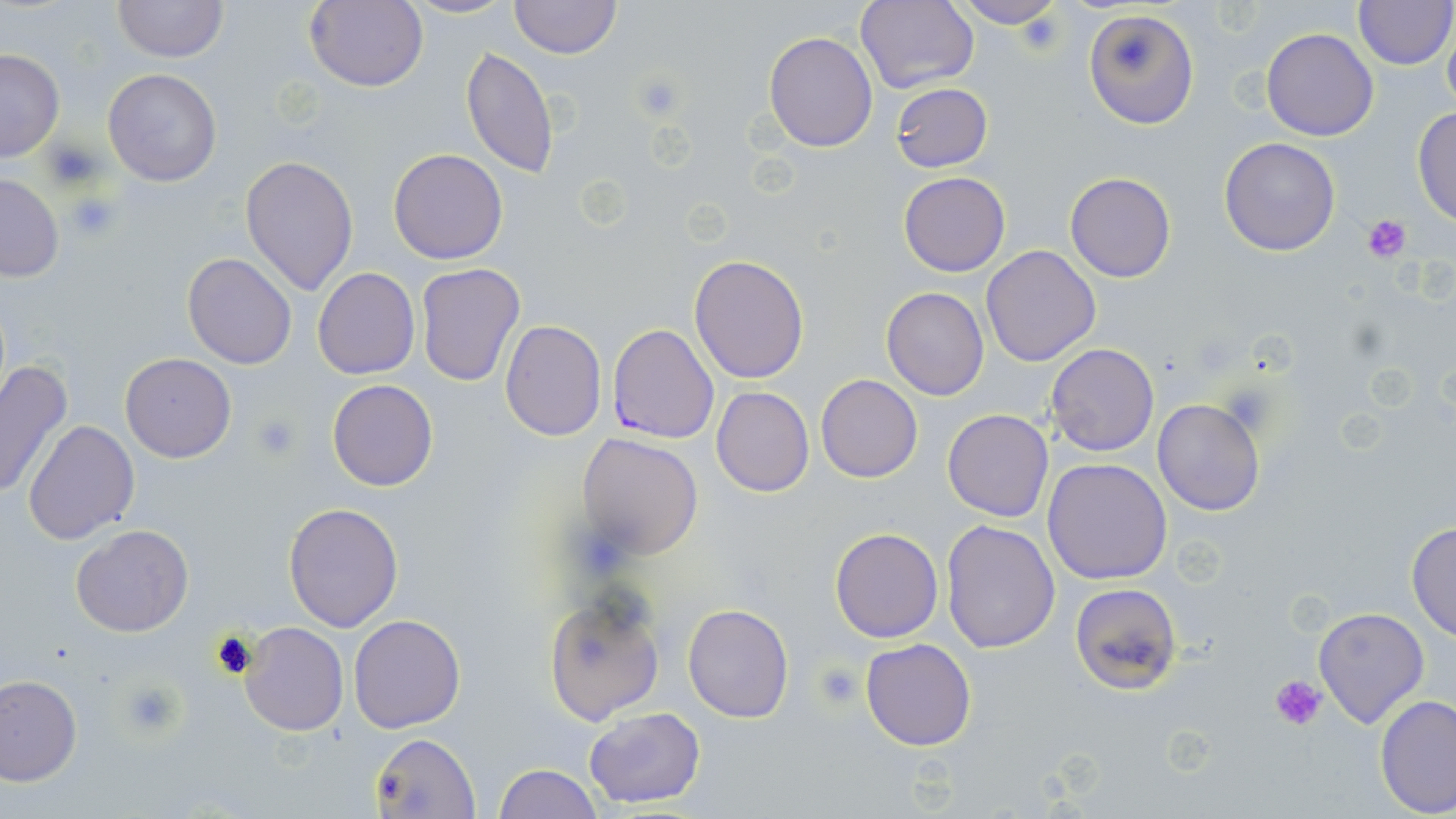
Summary:
  - Coordinate format: approximate bounding boxes as (x1,y1)-(x2,y2) corner pairs in pixels
  - Plasmodium falciparum-infected red blood cell locations: (609,323)-(717,444)
  - Platelet locations: (631,69)-(686,121), (43,136)-(106,189), (64,189)-(124,244), (1360,212)-(1412,261), (252,413)-(304,462), (815,662)-(863,710), (1270,675)-(1327,730), (116,679)-(186,740)
  - Uninfected red blood cell locations: (111,0)-(227,64), (303,0)-(428,92), (399,0)-(517,20), (508,0)-(622,57), (948,0)-(1069,28), (1353,0)-(1454,70), (856,1)-(981,95), (1084,9)-(1199,131), (1442,18)-(1456,114), (1262,28)-(1379,142), (763,31)-(878,151), (460,46)-(560,180), (0,49)-(65,162), (102,67)-(223,186), (890,81)-(993,172), (1412,106)-(1456,226), (1219,136)-(1341,257), (388,148)-(508,264), (240,153)-(359,295), (898,172)-(1010,276), (1065,172)-(1175,283), (0,174)-(64,282), (981,245)-(1103,366), (182,252)-(298,369), (688,254)-(810,384), (415,262)-(524,389), (313,267)-(420,379), (881,286)-(989,400), (501,320)-(606,440), (1046,343)-(1159,457), (120,353)-(236,462), (0,360)-(73,503), (816,374)-(923,483), (327,379)-(440,492), (711,387)-(814,496), (1152,397)-(1265,517), (941,409)-(1054,522), (23,420)-(142,545), (578,433)-(704,560), (1042,458)-(1173,586), (283,502)-(403,632), (939,519)-(1062,653), (1407,520)-(1456,643), (70,525)-(193,638), (830,528)-(943,642), (1069,582)-(1183,695), (543,594)-(665,727), (682,602)-(795,722), (1313,607)-(1429,726), (348,613)-(466,733), (240,622)-(348,735), (861,638)-(976,750), (0,673)-(82,785), (1375,693)-(1456,818), (583,707)-(706,809), (371,733)-(483,818), (494,764)-(602,819)
  - Slide-level diagnosis: Plasmodium falciparum
  - Modality: light microscopy
  - Stain: May-Grünwald-Giemsa
  - Image size: 1456×819 pixels
  - Magnification: 1000x
  - Field of view: single
  - Preparation: thin blood smear